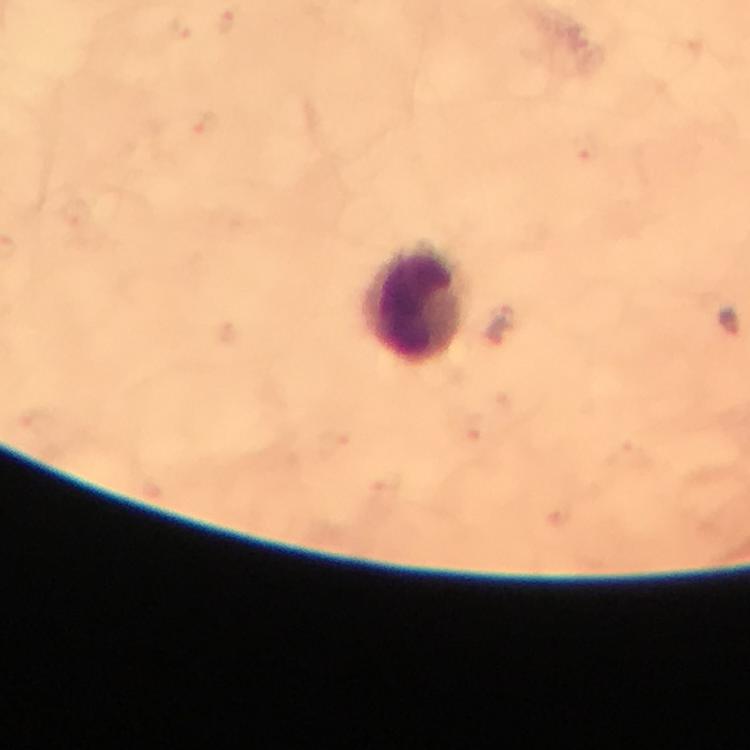 Approximate object centers, in pixels from the top-left corner. Leukocyte locations: (x=417, y=303). From a malaria diagnostic workup. Giemsa stain. Smartphone photograph taken through a microscope. Immersion oil was used. A crop from one field of view. Image is 750×750 pixels. At 100x magnification. Thick blood smear. Plasmodium parasites: none seen.